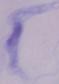 A trypanosome is shown. Photomicrograph. Captured at 1000x magnification.